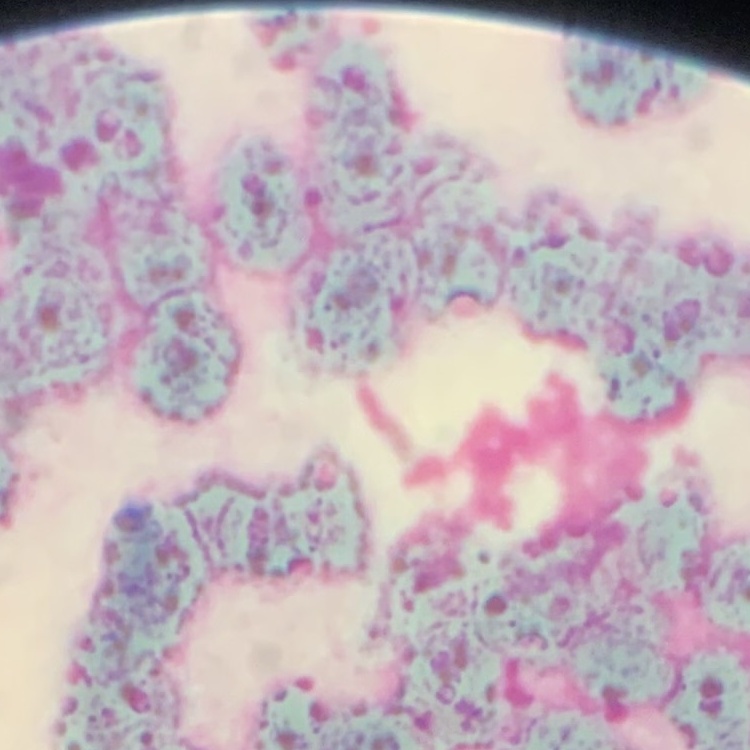

The erythrocytes show rouleaux formation. Stained with either Field's or Giemsa. Square crop of a larger photomicrograph. Thin blood film.